Locate every Plasmodium parasite.
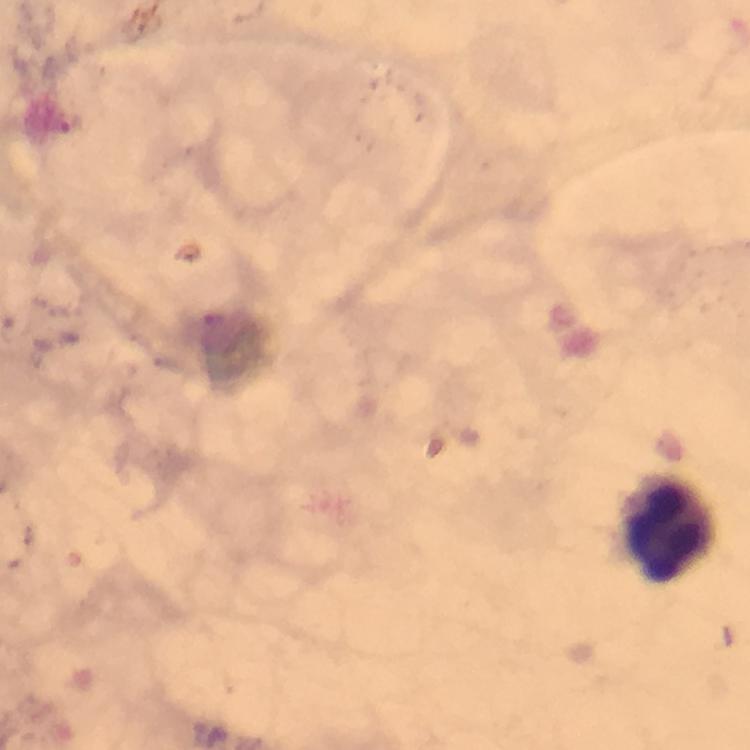
No Plasmodium parasites detected.

Approximate centers as (x, y) in pixels.
Summary:
  - Leukocyte locations: (672, 529)
  - Capture: smartphone photograph through a microscope
  - Image size: 750×750 pixels
  - Immersion oil: applied
  - Magnification: 100x
  - Stain: Giemsa
  - Cropped from: a single field of view
  - Context: from a malaria diagnostic workup
  - Preparation: thick blood film